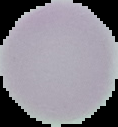 Image is 118×127 pixels. Segmented cell region on a black background. Result: negative for Plasmodium parasites. From a thin blood film.